Assess this cell for malaria.
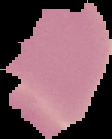
Uninfected.

Image is 112×139 pixels. From a thin blood smear. Cell region segmented out of the field of view; the surrounding area is masked to black.